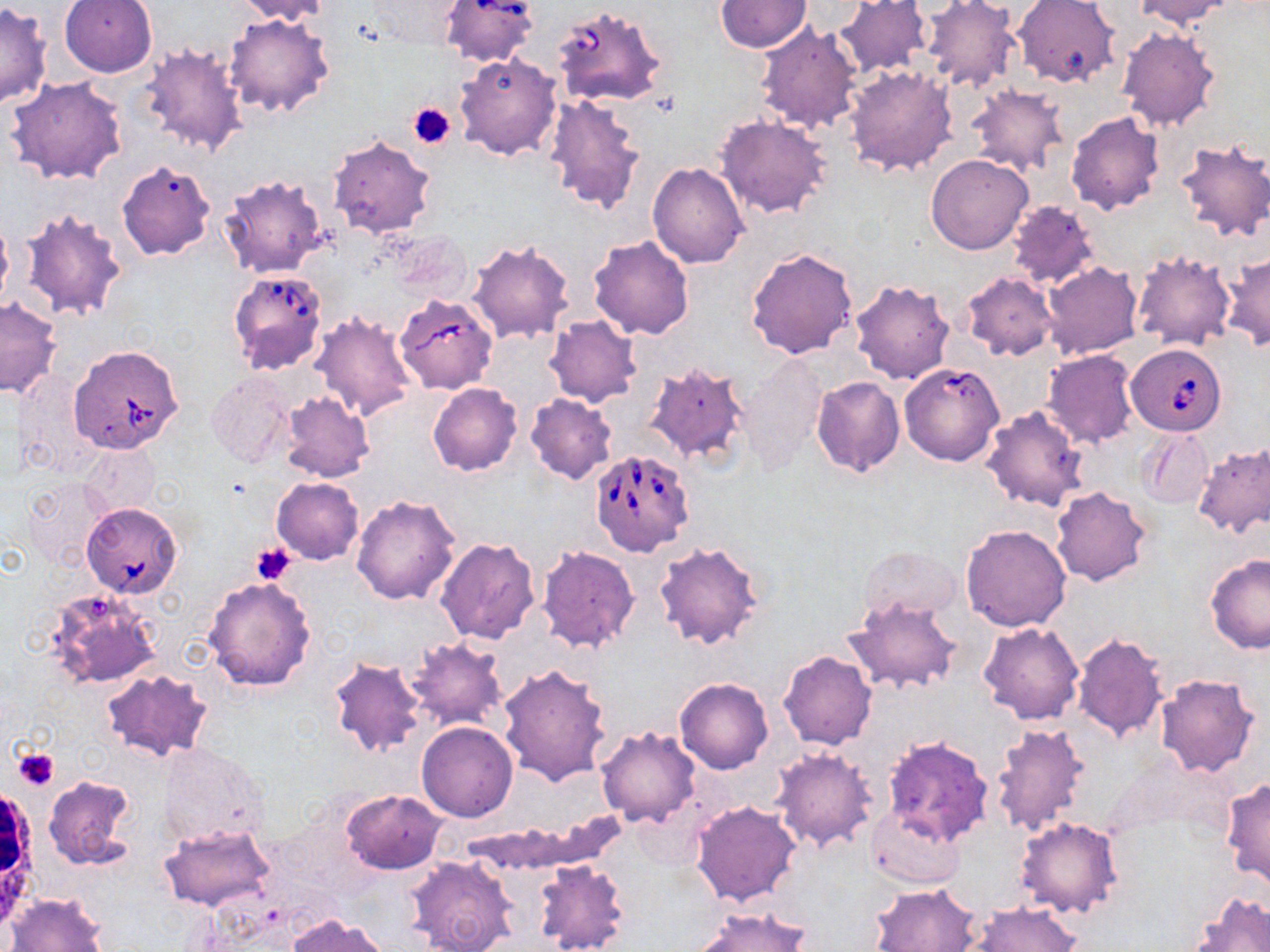

Summary:
  - Coordinate format: approximate bounding boxes as named x1/y1/x2/y2 corners in pixels
  - Babesia divergens-infected red blood cell locations: (x1=437, y1=0, x2=541, y2=68), (x1=550, y1=4, x2=668, y2=109), (x1=227, y1=268, x2=328, y2=374), (x1=393, y1=293, x2=497, y2=393), (x1=67, y1=344, x2=185, y2=455), (x1=1127, y1=344, x2=1226, y2=435), (x1=898, y1=362, x2=1006, y2=466), (x1=587, y1=448, x2=693, y2=555), (x1=81, y1=501, x2=184, y2=600)
  - Platelet locations: (x1=409, y1=102, x2=455, y2=148), (x1=252, y1=541, x2=297, y2=584), (x1=12, y1=748, x2=59, y2=791)
  - Uninfected red blood cell locations: (x1=58, y1=0, x2=157, y2=77), (x1=231, y1=0, x2=331, y2=23), (x1=834, y1=0, x2=932, y2=79), (x1=919, y1=0, x2=1020, y2=91), (x1=1012, y1=0, x2=1120, y2=88), (x1=1132, y1=0, x2=1235, y2=30), (x1=361, y1=1, x2=469, y2=50), (x1=715, y1=1, x2=810, y2=52), (x1=0, y1=3, x2=50, y2=110), (x1=224, y1=12, x2=336, y2=120), (x1=755, y1=22, x2=863, y2=134), (x1=1117, y1=26, x2=1220, y2=132), (x1=137, y1=44, x2=248, y2=159), (x1=453, y1=53, x2=561, y2=160), (x1=843, y1=64, x2=956, y2=177), (x1=6, y1=77, x2=129, y2=186), (x1=967, y1=83, x2=1069, y2=177), (x1=543, y1=95, x2=646, y2=213), (x1=1066, y1=111, x2=1165, y2=215), (x1=715, y1=114, x2=831, y2=219), (x1=327, y1=134, x2=436, y2=239), (x1=1173, y1=139, x2=1270, y2=243), (x1=925, y1=152, x2=1033, y2=254), (x1=117, y1=161, x2=215, y2=261), (x1=647, y1=162, x2=749, y2=268), (x1=218, y1=172, x2=330, y2=278), (x1=1006, y1=200, x2=1102, y2=289), (x1=19, y1=206, x2=128, y2=321), (x1=0, y1=216, x2=12, y2=316), (x1=387, y1=231, x2=473, y2=306), (x1=589, y1=236, x2=695, y2=340), (x1=467, y1=240, x2=574, y2=344), (x1=747, y1=247, x2=858, y2=360), (x1=1131, y1=251, x2=1235, y2=350), (x1=1223, y1=253, x2=1270, y2=352), (x1=1042, y1=262, x2=1142, y2=359), (x1=960, y1=272, x2=1059, y2=360), (x1=849, y1=278, x2=955, y2=384), (x1=0, y1=297, x2=62, y2=398), (x1=311, y1=310, x2=417, y2=421), (x1=545, y1=315, x2=641, y2=408), (x1=1043, y1=350, x2=1138, y2=448), (x1=738, y1=356, x2=828, y2=472), (x1=642, y1=361, x2=753, y2=467), (x1=206, y1=371, x2=297, y2=469), (x1=812, y1=375, x2=904, y2=476), (x1=427, y1=382, x2=522, y2=476), (x1=279, y1=391, x2=374, y2=483), (x1=525, y1=393, x2=617, y2=484), (x1=981, y1=405, x2=1089, y2=512), (x1=1138, y1=427, x2=1213, y2=510), (x1=1192, y1=440, x2=1269, y2=539), (x1=80, y1=442, x2=160, y2=519), (x1=21, y1=477, x2=109, y2=566), (x1=272, y1=477, x2=363, y2=564), (x1=1051, y1=487, x2=1151, y2=585), (x1=351, y1=494, x2=462, y2=606), (x1=960, y1=524, x2=1072, y2=632), (x1=434, y1=538, x2=541, y2=644), (x1=653, y1=539, x2=765, y2=651), (x1=535, y1=545, x2=640, y2=652), (x1=857, y1=546, x2=962, y2=624), (x1=1204, y1=555, x2=1270, y2=654), (x1=203, y1=574, x2=317, y2=691), (x1=43, y1=588, x2=160, y2=688), (x1=845, y1=595, x2=962, y2=695), (x1=978, y1=621, x2=1085, y2=725), (x1=1070, y1=631, x2=1169, y2=744), (x1=401, y1=636, x2=508, y2=733), (x1=778, y1=649, x2=877, y2=750), (x1=327, y1=656, x2=426, y2=759), (x1=499, y1=663, x2=611, y2=786), (x1=101, y1=668, x2=214, y2=764), (x1=1154, y1=673, x2=1261, y2=779), (x1=675, y1=677, x2=773, y2=774), (x1=416, y1=722, x2=518, y2=822), (x1=990, y1=722, x2=1092, y2=839), (x1=596, y1=726, x2=701, y2=827), (x1=882, y1=736, x2=995, y2=844), (x1=159, y1=744, x2=269, y2=849), (x1=770, y1=747, x2=878, y2=854), (x1=42, y1=776, x2=136, y2=869), (x1=1223, y1=779, x2=1270, y2=887), (x1=342, y1=789, x2=446, y2=874), (x1=691, y1=800, x2=802, y2=906), (x1=866, y1=802, x2=966, y2=889), (x1=1014, y1=815, x2=1125, y2=920), (x1=159, y1=823, x2=275, y2=912), (x1=406, y1=855, x2=518, y2=952), (x1=532, y1=859, x2=630, y2=952), (x1=870, y1=882, x2=982, y2=952), (x1=6, y1=892, x2=108, y2=952), (x1=1191, y1=893, x2=1270, y2=952), (x1=968, y1=902, x2=1080, y2=952), (x1=691, y1=905, x2=812, y2=952), (x1=288, y1=914, x2=387, y2=952)
  - White blood cell locations: (x1=0, y1=790, x2=43, y2=929)
  - Slide-level diagnosis: Babesia divergens
  - Field of view: single
  - Preparation: thin blood smear
  - Magnification: 1000x
  - Modality: light microscopy
  - Image size: 1270×952 pixels
  - Stain: May-Grünwald-Giemsa